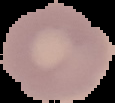
Summary:
  - Result: no malaria parasites detected
  - Preparation: thin blood film
  - Image type: segmented cell region on a black background
  - Image size: 115×103 pixels